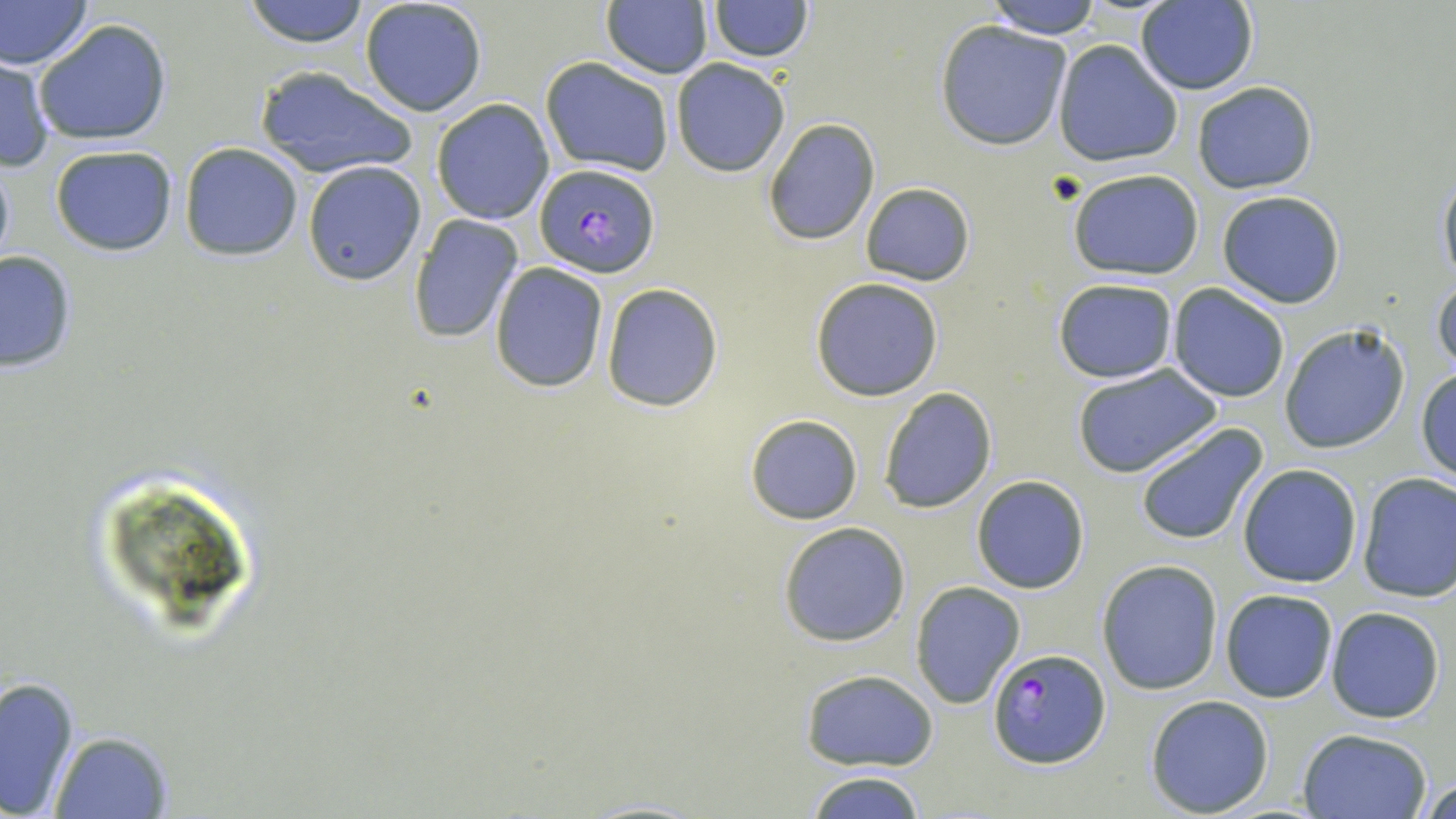

plasmodium_falciparum_infected_red_blood_cell_locations: 'approximate bounding boxes as (x1,y1)-(x2,y2) corner pairs in pixels: (533,163)-(663,277), (987,646)-(1112,769)'
slide_level_diagnosis: Plasmodium falciparum
preparation: thin blood film
modality: optical microscopy
stain: May-Grünwald-Giemsa
magnification: 1000x
field_of_view: single
image_size: 1456×819 pixels
uninfected_red_blood_cell_locations: 'approximate bounding boxes as (x1,y1)-(x2,y2) corner pairs in pixels: (244,0)-(369,47), (359,0)-(488,117), (707,0)-(814,62), (983,0)-(1103,37), (0,1)-(93,68), (601,1)-(714,79), (1135,1)-(1258,95), (32,18)-(173,146), (936,20)-(1072,149), (1053,40)-(1184,169), (0,56)-(55,172), (540,57)-(675,176), (670,59)-(789,176), (252,64)-(417,179), (1193,80)-(1318,194), (431,98)-(556,224), (763,117)-(881,244), (179,143)-(304,262), (48,144)-(179,257), (0,149)-(14,274), (302,160)-(427,286), (1437,165)-(1456,287), (1065,168)-(1208,279), (859,181)-(976,287), (1216,190)-(1346,309), (407,215)-(525,342), (0,250)-(76,374), (491,262)-(607,392), (1431,272)-(1455,378), (810,276)-(944,402), (1052,278)-(1178,384), (600,283)-(723,413), (1167,283)-(1290,403), (1279,322)-(1411,455), (1074,365)-(1221,478), (1416,367)-(1456,484), (879,386)-(997,513), (745,414)-(862,525), (1133,422)-(1268,546), (1237,463)-(1364,588), (1356,472)-(1455,602), (971,476)-(1090,593), (778,521)-(911,646), (1096,559)-(1223,694), (910,582)-(1026,710), (1219,588)-(1338,704), (1326,606)-(1446,724), (800,670)-(938,772), (0,673)-(82,817), (1145,694)-(1274,817), (1296,729)-(1432,818), (54,733)-(169,819), (806,769)-(928,818), (1421,775)-(1454,817)'